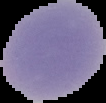
{
  "malaria_status": "uninfected",
  "image_size": "106×103 pixels",
  "image_type": "cell region segmented out of the field of view; surrounding area masked to black",
  "preparation": "thin blood smear"
}